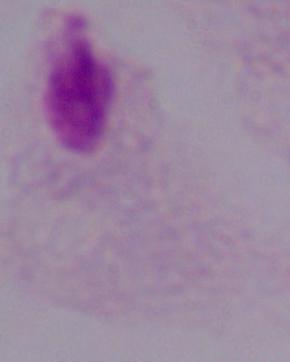
modality = micrograph
magnification = 1000x
identification = trichomonad